Comment on the morphology of the erythrocytes.
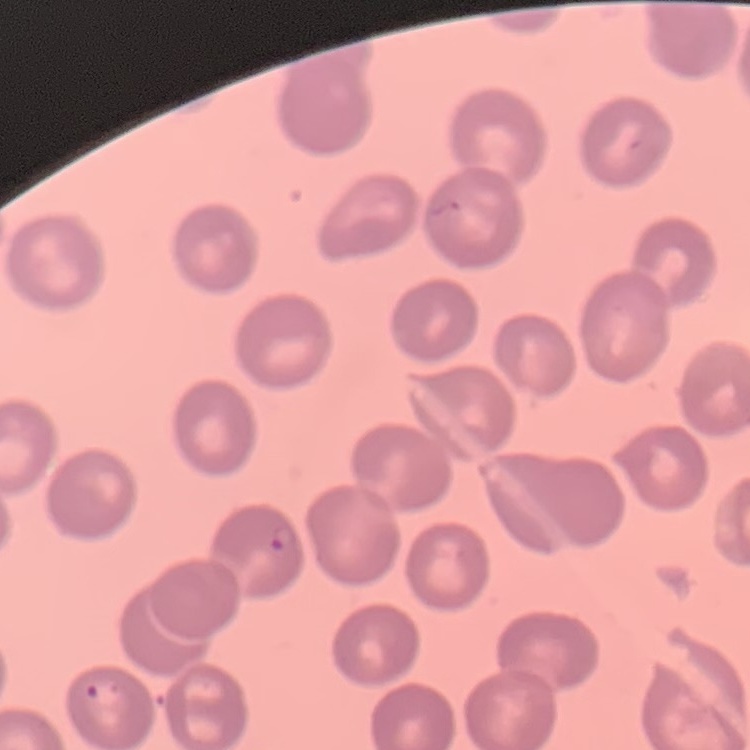

They show no rouleaux formation.

Field's or Giemsa stain. Thin blood smear. One tile cut from a larger photomicrograph.